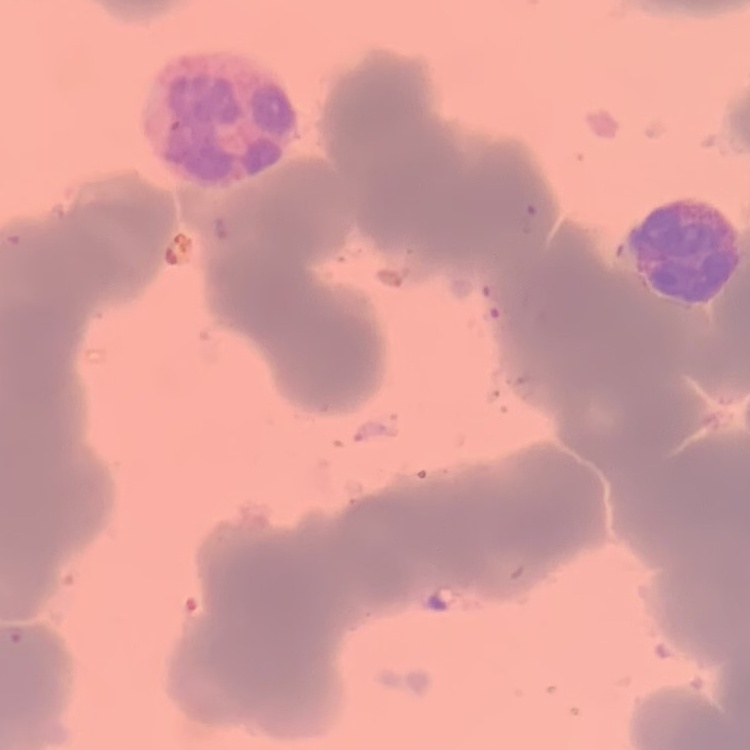
The erythrocytes exhibit rouleaux formation. Stained with either Field's or Giemsa. Square crop of a larger photomicrograph. Thin peripheral smear.